Locate every Plasmodium ovale-infected red blood cell.
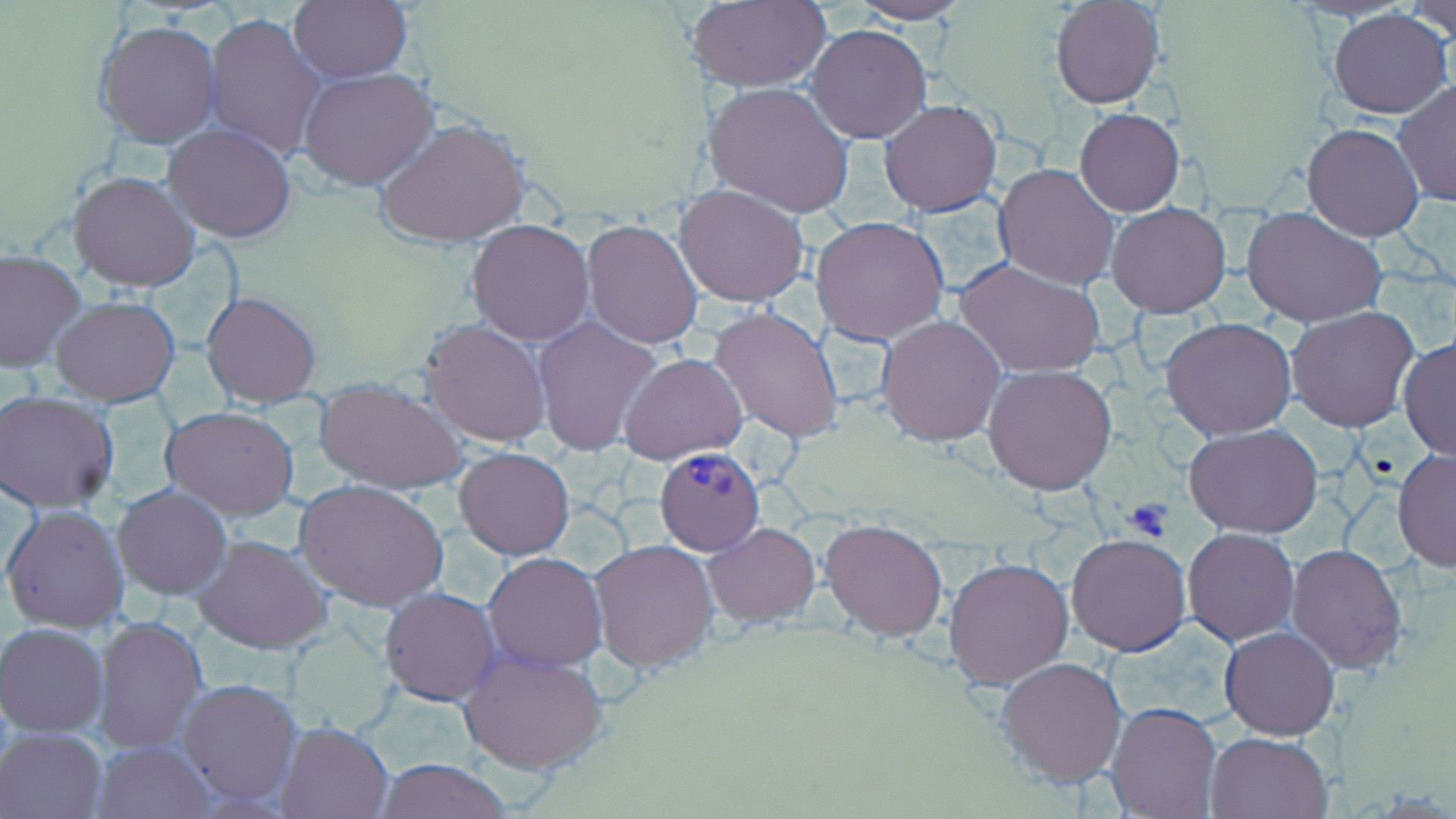

Approximate bounding boxes as [x1, y1, x2, y2] in pixels.
Plasmodium ovale-infected red blood cells: [654, 445, 765, 556].

slide-level diagnosis = Plasmodium ovale
image size = 1456×819 pixels
modality = optical microscopy
uninfected red blood cell locations = approximate bounding boxes as [x1, y1, x2, y2] in pixels: [289, 0, 412, 83], [684, 1, 831, 91], [1051, 1, 1164, 108], [1401, 1, 1456, 45], [849, 2, 971, 24], [1327, 8, 1453, 118], [204, 12, 327, 161], [94, 19, 223, 149], [806, 24, 932, 144], [299, 67, 439, 191], [1392, 79, 1456, 206], [705, 81, 857, 218], [879, 99, 1003, 216], [1075, 107, 1184, 216], [376, 117, 529, 247], [1302, 123, 1424, 241], [162, 124, 296, 243], [995, 162, 1120, 291], [68, 170, 200, 293], [675, 187, 810, 307], [1107, 202, 1231, 317], [1242, 205, 1388, 327], [811, 215, 949, 344], [582, 220, 704, 350], [466, 221, 595, 346], [0, 249, 86, 373], [954, 256, 1106, 380], [201, 289, 323, 408], [51, 296, 181, 405], [1286, 305, 1421, 432], [707, 307, 844, 444], [877, 314, 1005, 446], [532, 316, 660, 456], [1160, 317, 1298, 440], [421, 318, 550, 446], [1398, 337, 1456, 459], [620, 351, 748, 463], [984, 365, 1118, 495], [316, 378, 467, 495], [1, 389, 120, 513], [161, 406, 299, 519], [1184, 424, 1323, 537], [455, 447, 574, 559], [1392, 449, 1455, 572], [297, 479, 449, 611], [114, 484, 233, 600], [3, 504, 130, 633], [819, 519, 948, 640], [703, 522, 820, 627], [1183, 527, 1299, 646], [194, 533, 333, 654], [1067, 533, 1191, 655], [587, 538, 718, 672], [1286, 543, 1409, 673], [484, 552, 607, 671], [944, 555, 1074, 690], [380, 588, 500, 706], [94, 613, 208, 753], [1, 621, 111, 735], [1220, 626, 1339, 739], [459, 648, 610, 775], [997, 657, 1128, 788], [177, 677, 302, 807], [1106, 701, 1222, 817], [277, 720, 394, 818], [1, 726, 107, 818], [1205, 733, 1334, 819], [94, 740, 214, 818], [375, 759, 516, 818]
stain = May-Grünwald-Giemsa
magnification = 1000x
field of view = single
platelet locations = approximate bounding boxes as [x1, y1, x2, y2] in pixels: [1123, 496, 1177, 541]
preparation = thin blood film